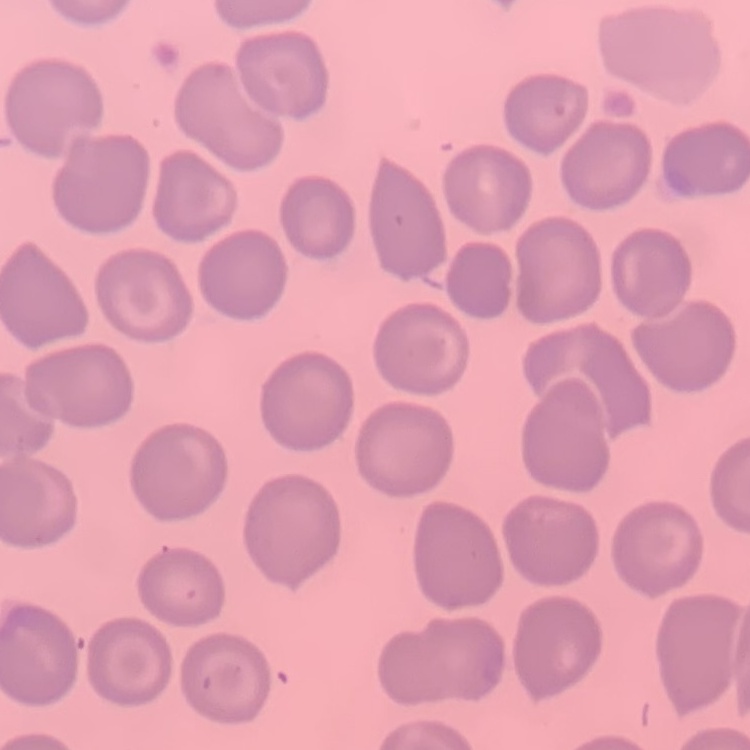
Summary:
  - Red blood cell morphology: no rouleaux formation
  - Image type: one tile cut from a larger photomicrograph
  - Preparation: thin blood film
  - Stain: Field's or Giemsa